Describe the morphology of the red blood cells.
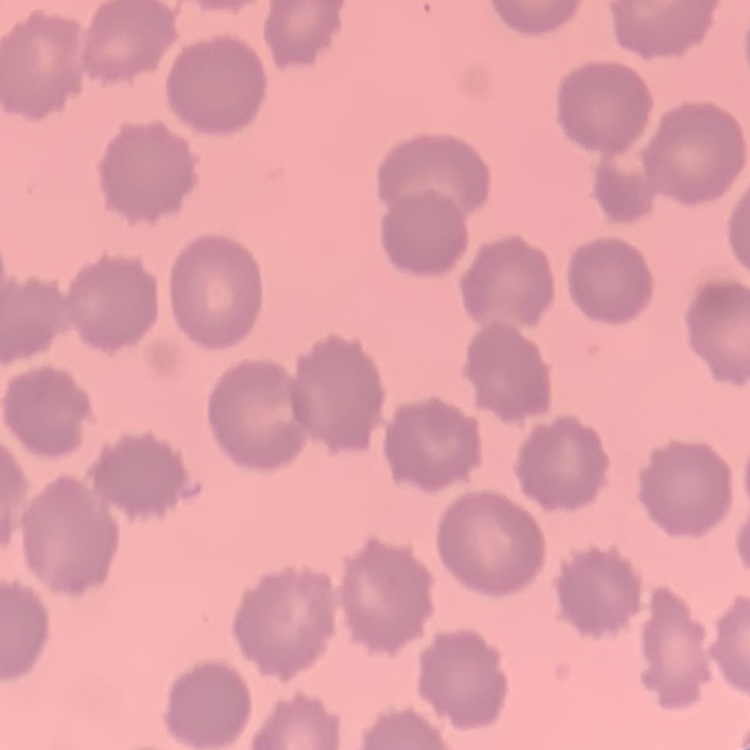
They show no rouleaux formation.

image type = square crop of a larger photomicrograph
stain = Field's or Giemsa
preparation = thin blood smear